Assess the morphology of the red blood cells.
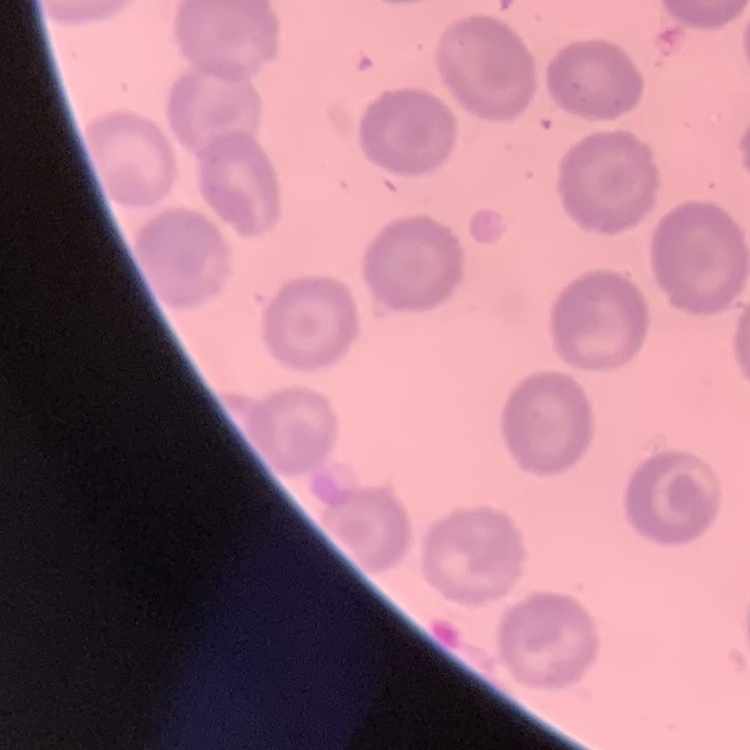

No rouleaux formation.

Field's or Giemsa stain. Thin peripheral smear. One tile cut from a larger photomicrograph.